Locate every blood parasite and identify its species.
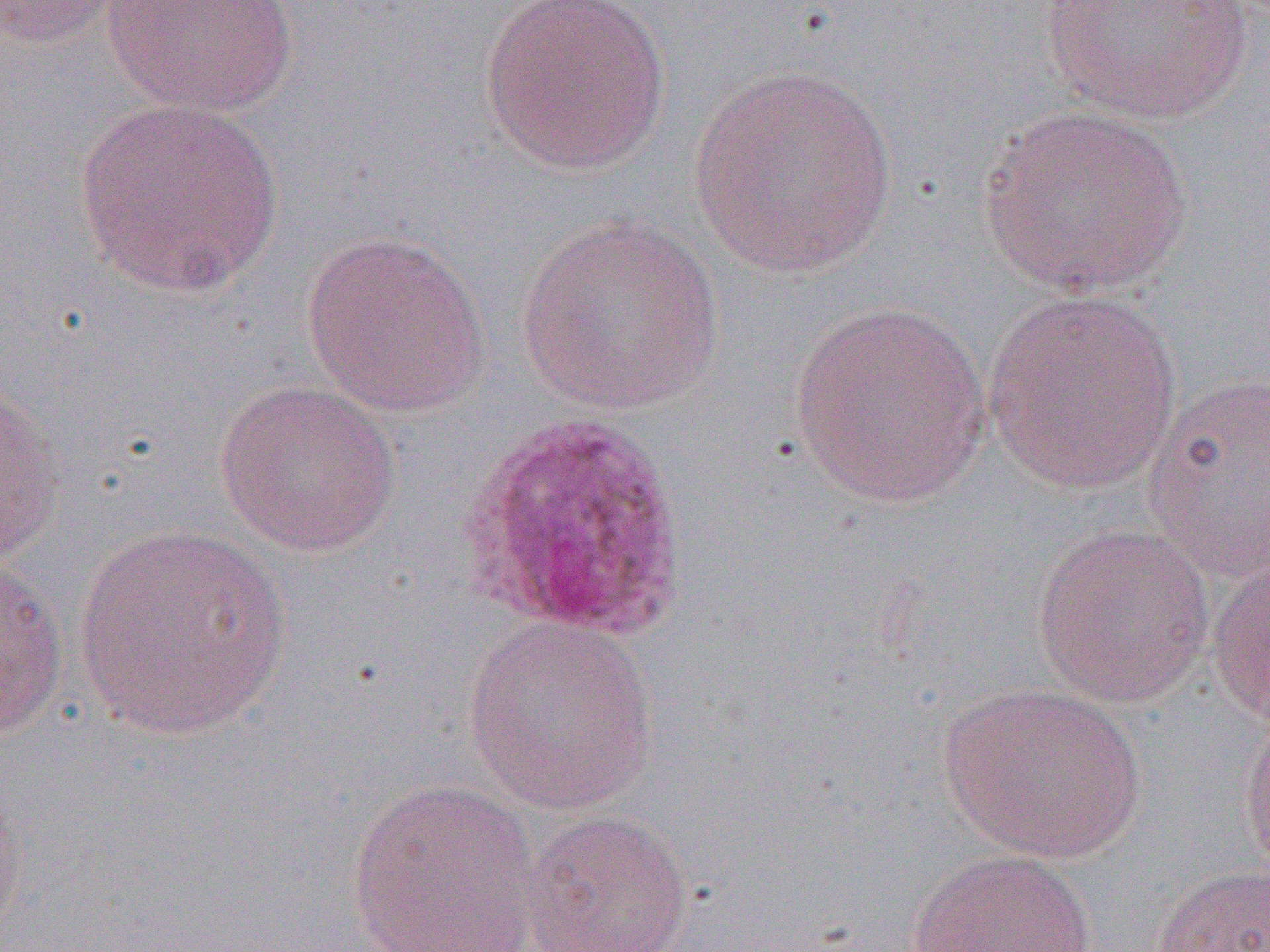

Approximate bounding boxes as [x1, y1, x2, y2] in pixels.
Plasmodium ovale-infected red blood cells: [459, 408, 692, 643].
No Plasmodium falciparum, Plasmodium malariae, Plasmodium vivax, Babesia divergens, or Trypanosoma brucei observed.

Uninfected red blood cell locations: [0, 0, 134, 49], [102, 0, 301, 116], [479, 1, 672, 176], [1037, 1, 1255, 125], [688, 66, 899, 279], [73, 97, 286, 300], [978, 103, 1193, 298], [514, 212, 723, 416], [300, 229, 493, 418], [982, 288, 1183, 495], [789, 299, 993, 509], [1141, 372, 1270, 582], [212, 379, 402, 557], [0, 381, 67, 569], [1031, 523, 1215, 707], [71, 525, 292, 740], [0, 554, 68, 746], [1206, 554, 1269, 728], [463, 616, 659, 814], [936, 683, 1145, 863], [1237, 708, 1270, 881], [0, 771, 26, 948], [345, 778, 544, 952], [520, 808, 694, 952], [907, 848, 1098, 952], [1152, 862, 1270, 952]. Slide-level diagnosis: Plasmodium ovale. Single field of view. 1000x magnification. Thin blood film. Image is 1270×952 pixels. Light microscopy.